Locate every blood parasite and identify its species.
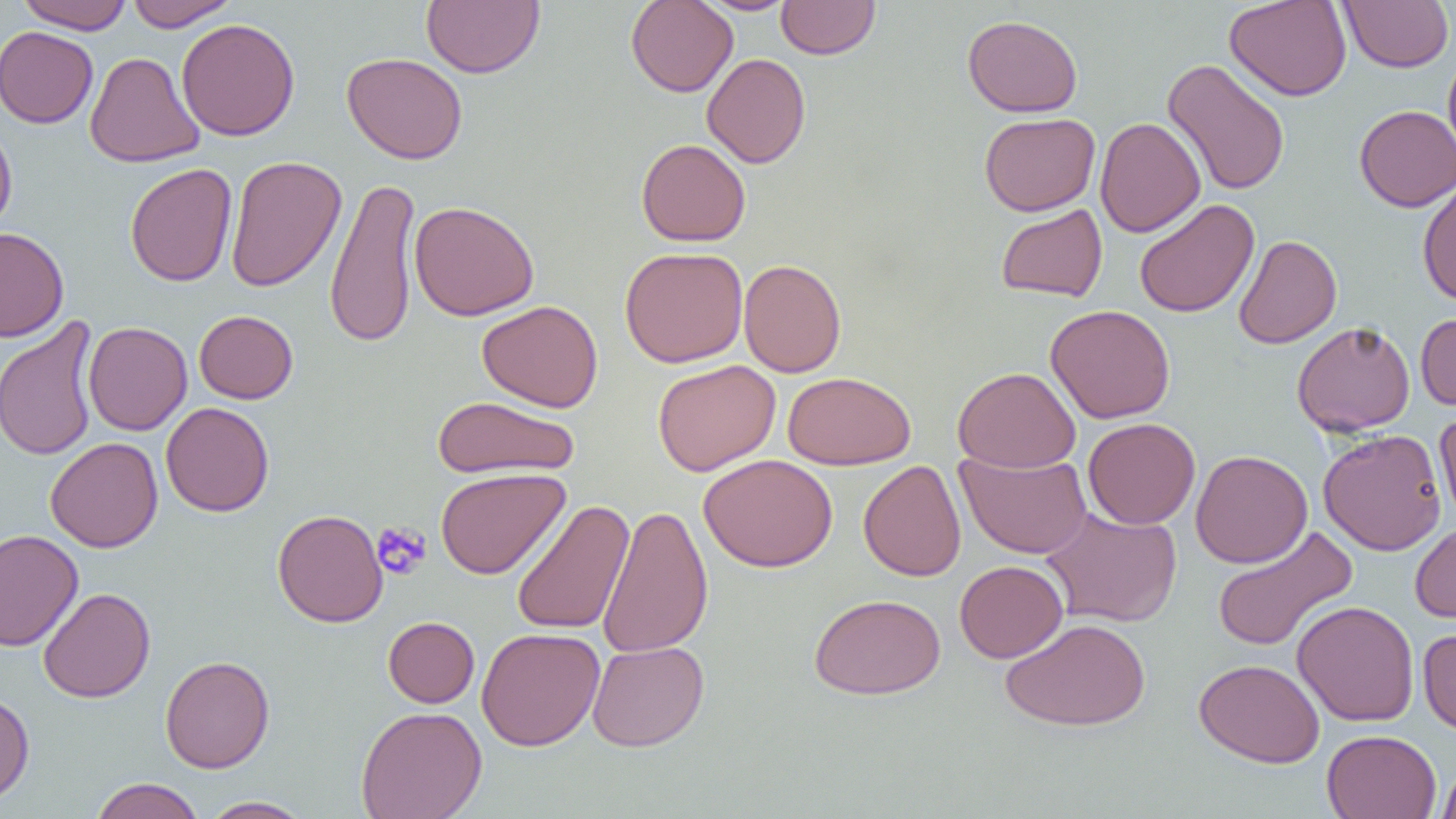

No blood parasites observed.

{
  "slide_level_diagnosis": "negative for blood parasites",
  "uninfected_red_blood_cell_locations": "approximate bounding boxes as (x1,y1)-(x2,y2) corner pairs in pixels: (17,0)-(134,33), (123,0)-(240,30), (421,0)-(544,78), (625,0)-(738,97), (1224,0)-(1352,101), (1340,0)-(1453,72), (696,1)-(799,15), (776,1)-(880,59), (962,14)-(1083,117), (176,18)-(301,142), (0,26)-(98,128), (1443,50)-(1456,165), (85,51)-(205,168), (341,52)-(468,164), (701,52)-(811,168), (1162,59)-(1290,196), (1354,105)-(1456,211), (979,112)-(1100,216), (1094,116)-(1205,238), (0,119)-(18,235), (636,139)-(751,247), (225,155)-(346,292), (124,163)-(237,287), (325,174)-(421,349), (1417,180)-(1456,306), (1134,199)-(1259,318), (409,200)-(539,321), (995,203)-(1108,302), (0,226)-(69,341), (1233,234)-(1342,349), (619,246)-(748,368), (738,259)-(847,377), (477,300)-(603,412), (1045,304)-(1175,424), (194,310)-(298,404), (1416,311)-(1456,411), (0,314)-(100,463), (83,321)-(193,435), (1291,321)-(1415,437), (652,360)-(781,476), (953,366)-(1081,472), (783,371)-(916,470), (432,395)-(580,480), (161,401)-(274,517), (1434,409)-(1456,528), (1083,417)-(1201,529), (1319,429)-(1446,556), (45,437)-(163,553), (955,450)-(1092,559), (1190,450)-(1313,569), (699,453)-(838,572), (858,460)-(966,582), (435,468)-(571,580), (511,500)-(635,636), (596,503)-(714,658), (1041,506)-(1182,627), (272,509)-(388,627), (1410,521)-(1456,623), (1211,526)-(1359,653), (0,529)-(83,651), (954,560)-(1068,663), (38,587)-(155,703), (809,593)-(945,700), (1292,600)-(1419,726), (383,616)-(480,708), (1000,618)-(1151,731), (476,627)-(605,751), (1418,628)-(1456,735), (587,640)-(709,752), (160,655)-(275,773), (1194,658)-(1325,768), (0,689)-(35,805), (356,705)-(487,819), (1322,730)-(1441,819), (1437,762)-(1456,818), (89,778)-(205,819), (199,796)-(313,818)",
  "modality": "light microscopy",
  "magnification": "1000x",
  "platelet_locations": "approximate bounding boxes as (x1,y1)-(x2,y2) corner pairs in pixels: (372,522)-(431,580)",
  "field_of_view": "one of a larger specimen",
  "image_size": "1456×819 pixels",
  "preparation": "thin blood smear"
}